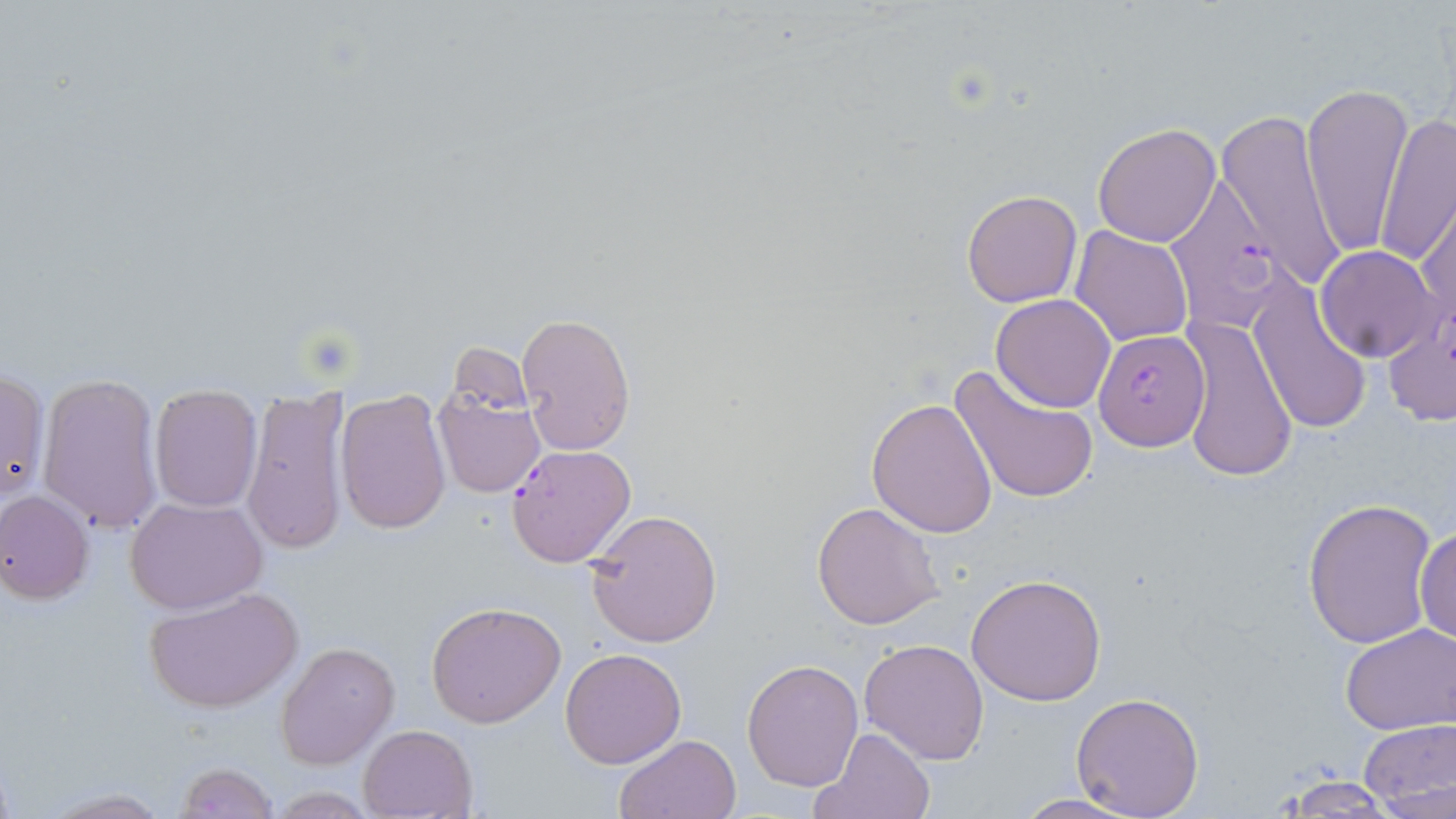
{
  "slide_level_diagnosis": "Plasmodium falciparum",
  "field_of_view": "one of a larger specimen",
  "preparation": "thin blood smear",
  "stain": "May-Grünwald-Giemsa",
  "uninfected_red_blood_cell_locations": "approximate bounding boxes as named x1/y1/x2/y2 corners in pixels: (x1=1301, y1=80, x2=1412, y2=258), (x1=1216, y1=109, x2=1348, y2=292), (x1=1375, y1=110, x2=1456, y2=268), (x1=1092, y1=122, x2=1222, y2=247), (x1=962, y1=189, x2=1082, y2=307), (x1=1416, y1=193, x2=1455, y2=343), (x1=1072, y1=226, x2=1192, y2=347), (x1=1317, y1=245, x2=1442, y2=363), (x1=1247, y1=278, x2=1374, y2=438), (x1=991, y1=294, x2=1115, y2=412), (x1=517, y1=313, x2=636, y2=454), (x1=1176, y1=314, x2=1300, y2=484), (x1=1381, y1=316, x2=1456, y2=429), (x1=951, y1=364, x2=1100, y2=506), (x1=0, y1=368, x2=49, y2=502), (x1=38, y1=373, x2=165, y2=534), (x1=149, y1=386, x2=263, y2=511), (x1=434, y1=387, x2=546, y2=496), (x1=242, y1=389, x2=353, y2=557), (x1=335, y1=389, x2=452, y2=533), (x1=866, y1=397, x2=999, y2=539), (x1=1, y1=490, x2=95, y2=603), (x1=126, y1=497, x2=267, y2=614), (x1=1301, y1=497, x2=1439, y2=648), (x1=812, y1=501, x2=944, y2=631), (x1=583, y1=507, x2=722, y2=648), (x1=1415, y1=519, x2=1455, y2=649), (x1=966, y1=572, x2=1107, y2=706), (x1=144, y1=585, x2=304, y2=712), (x1=426, y1=601, x2=566, y2=727), (x1=1339, y1=622, x2=1455, y2=734), (x1=860, y1=638, x2=989, y2=765), (x1=275, y1=641, x2=399, y2=768), (x1=559, y1=646, x2=687, y2=768), (x1=742, y1=658, x2=864, y2=792), (x1=1070, y1=689, x2=1205, y2=818), (x1=1358, y1=718, x2=1455, y2=814), (x1=357, y1=725, x2=477, y2=818), (x1=806, y1=727, x2=935, y2=819), (x1=614, y1=733, x2=741, y2=818), (x1=174, y1=761, x2=279, y2=818), (x1=1276, y1=774, x2=1399, y2=815), (x1=38, y1=787, x2=174, y2=818), (x1=1006, y1=793, x2=1147, y2=819)",
  "magnification": "1000x",
  "image_size": "1456×819 pixels",
  "modality": "optical microscopy",
  "plasmodium_falciparum_infected_red_blood_cell_locations": "approximate bounding boxes as named x1/y1/x2/y2 corners in pixels: (x1=1161, y1=174, x2=1289, y2=331), (x1=1094, y1=331, x2=1211, y2=452), (x1=508, y1=444, x2=636, y2=568)"
}